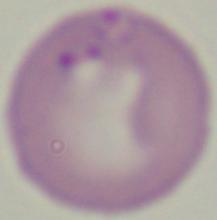

identification = Babesia
modality = photomicrograph
magnification = 1000x